Assess this cell for malaria.
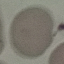

It is uninfected.

Summary:
  - Image type: cell patch, automatically extracted from a larger field of view and resized to 64 × 64 pixels
  - Stain: Giemsa
  - Preparation: thin smear
  - Capture: smartphone through the microscope eyepiece